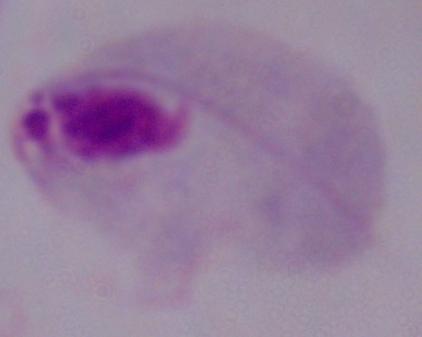
Summary:
  - Identification: trichomonad
  - Modality: micrograph
  - Magnification: 1000x